Locate and identify every blood parasite.
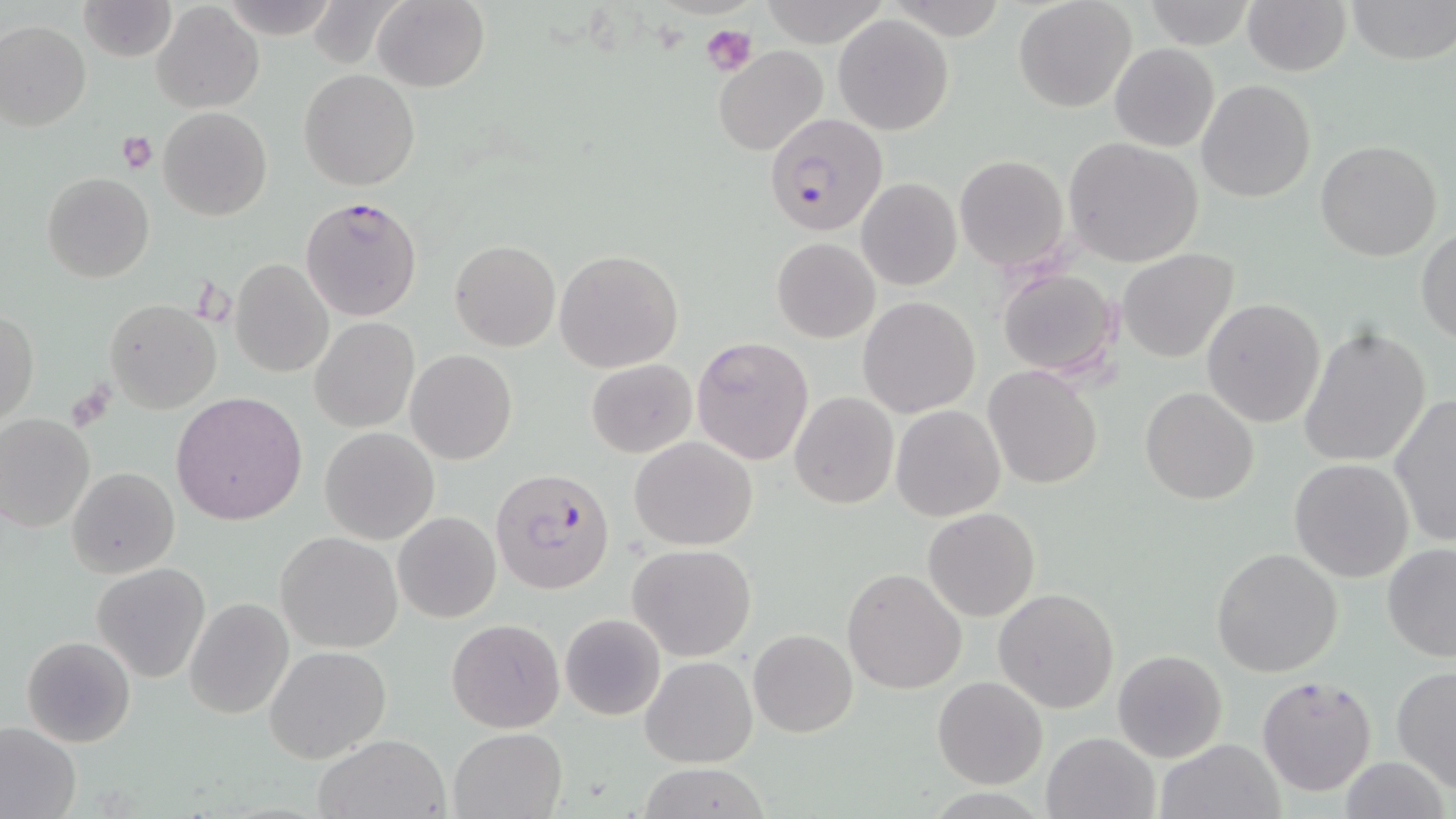

Approximate bounding boxes as named x1/y1/x2/y2 corners in pixels.
Plasmodium falciparum-infected red blood cells: (x1=763, y1=112, x2=888, y2=236), (x1=300, y1=195, x2=423, y2=322), (x1=490, y1=466, x2=617, y2=595).
No Plasmodium ovale, Plasmodium malariae, Plasmodium vivax, Babesia divergens, or Trypanosoma brucei observed.

Platelet locations: (x1=701, y1=24, x2=756, y2=75), (x1=117, y1=131, x2=158, y2=174). Uninfected red blood cell locations: (x1=79, y1=0, x2=178, y2=62), (x1=372, y1=0, x2=489, y2=92), (x1=1014, y1=0, x2=1138, y2=113), (x1=1242, y1=0, x2=1352, y2=75), (x1=1347, y1=0, x2=1455, y2=64), (x1=756, y1=1, x2=888, y2=45), (x1=1143, y1=2, x2=1254, y2=48), (x1=152, y1=3, x2=262, y2=115), (x1=833, y1=14, x2=955, y2=135), (x1=0, y1=20, x2=91, y2=131), (x1=1109, y1=43, x2=1219, y2=152), (x1=714, y1=47, x2=829, y2=157), (x1=299, y1=69, x2=419, y2=191), (x1=1196, y1=79, x2=1316, y2=203), (x1=157, y1=106, x2=272, y2=221), (x1=1064, y1=137, x2=1206, y2=266), (x1=1315, y1=138, x2=1441, y2=262), (x1=956, y1=156, x2=1069, y2=270), (x1=43, y1=173, x2=154, y2=283), (x1=856, y1=177, x2=961, y2=291), (x1=1415, y1=227, x2=1456, y2=344), (x1=772, y1=237, x2=879, y2=343), (x1=449, y1=240, x2=561, y2=352), (x1=554, y1=249, x2=683, y2=374), (x1=1117, y1=249, x2=1239, y2=363), (x1=230, y1=257, x2=334, y2=377), (x1=994, y1=266, x2=1122, y2=381), (x1=858, y1=297, x2=980, y2=418), (x1=1201, y1=297, x2=1326, y2=428), (x1=104, y1=298, x2=221, y2=413), (x1=1, y1=310, x2=39, y2=424), (x1=311, y1=318, x2=419, y2=433), (x1=1298, y1=324, x2=1432, y2=469), (x1=306, y1=333, x2=513, y2=448), (x1=691, y1=337, x2=814, y2=465), (x1=406, y1=349, x2=517, y2=464), (x1=587, y1=358, x2=697, y2=457), (x1=983, y1=365, x2=1104, y2=488), (x1=1138, y1=385, x2=1261, y2=505), (x1=173, y1=391, x2=308, y2=525), (x1=789, y1=392, x2=900, y2=511), (x1=1388, y1=395, x2=1456, y2=547), (x1=890, y1=404, x2=1005, y2=521), (x1=0, y1=413, x2=95, y2=533), (x1=321, y1=427, x2=439, y2=544), (x1=631, y1=436, x2=758, y2=550), (x1=1288, y1=459, x2=1414, y2=583), (x1=1232, y1=462, x2=1391, y2=633), (x1=68, y1=467, x2=179, y2=579), (x1=923, y1=507, x2=1039, y2=622), (x1=393, y1=510, x2=500, y2=623), (x1=275, y1=531, x2=402, y2=653), (x1=629, y1=544, x2=755, y2=661), (x1=1381, y1=544, x2=1456, y2=663), (x1=1211, y1=548, x2=1342, y2=678), (x1=92, y1=564, x2=210, y2=682), (x1=842, y1=568, x2=967, y2=695), (x1=994, y1=588, x2=1120, y2=713), (x1=184, y1=596, x2=294, y2=720), (x1=559, y1=613, x2=667, y2=721), (x1=446, y1=618, x2=564, y2=733), (x1=748, y1=629, x2=857, y2=738), (x1=22, y1=636, x2=136, y2=747), (x1=264, y1=645, x2=391, y2=763), (x1=1113, y1=648, x2=1227, y2=763), (x1=640, y1=655, x2=757, y2=768), (x1=1391, y1=667, x2=1456, y2=791), (x1=1256, y1=675, x2=1377, y2=797), (x1=932, y1=677, x2=1049, y2=789), (x1=0, y1=720, x2=81, y2=819), (x1=448, y1=728, x2=565, y2=818), (x1=1041, y1=731, x2=1162, y2=819), (x1=314, y1=733, x2=449, y2=819), (x1=1157, y1=738, x2=1284, y2=819), (x1=1339, y1=756, x2=1451, y2=819), (x1=634, y1=763, x2=774, y2=818). Slide-level diagnosis: Plasmodium falciparum. Image is 1456×819 pixels. Single field of view. May-Grünwald-Giemsa stain. Light microscopy. 1000x magnification. Thin blood film.